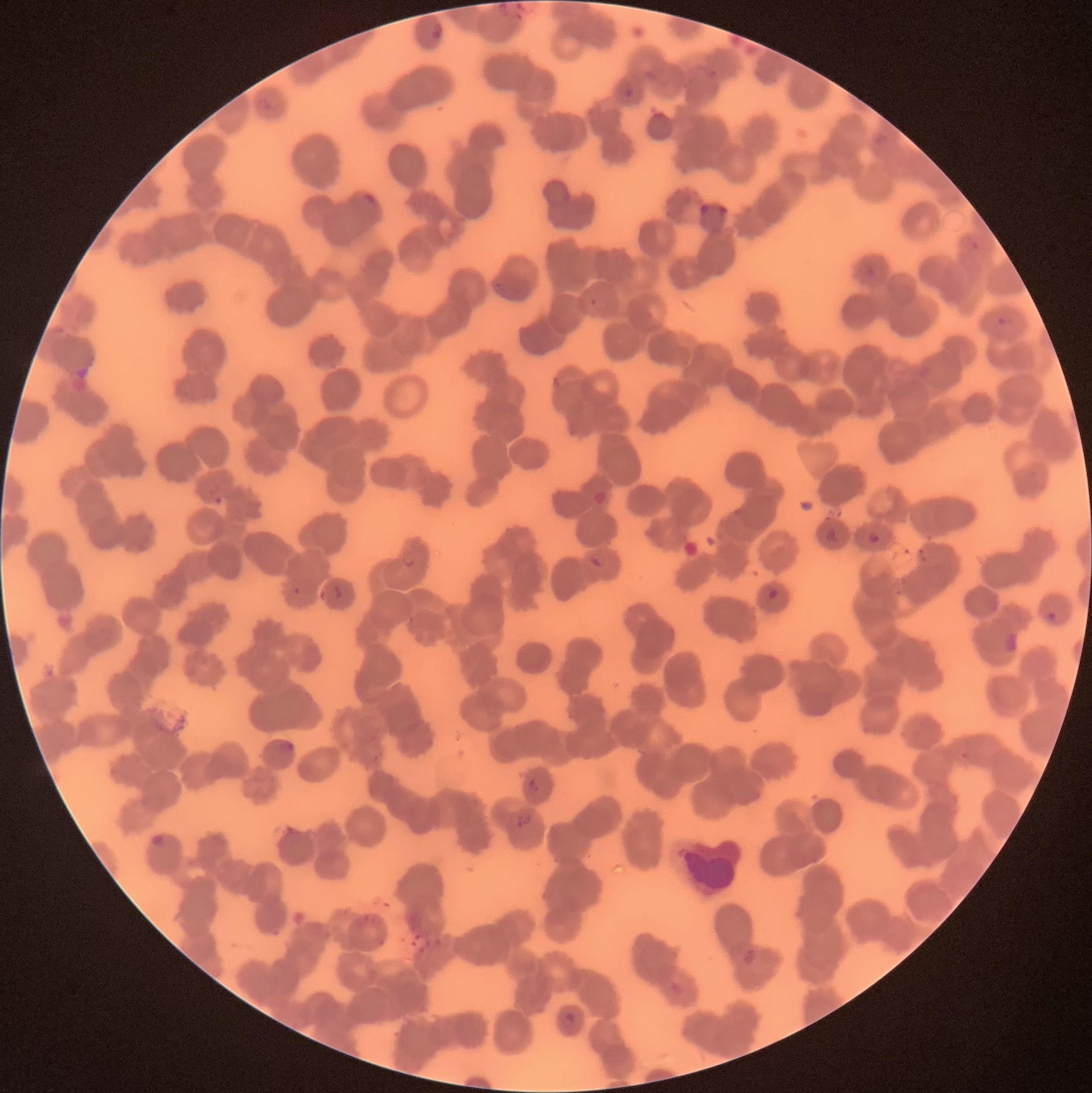

coordinate format = approximate bounding boxes as named x1/y1/x2/y2 corners in pixels
Plasmodium parasite locations = (x1=496, y1=2, x2=513, y2=18), (x1=430, y1=23, x2=444, y2=41), (x1=702, y1=64, x2=719, y2=79), (x1=615, y1=81, x2=635, y2=99), (x1=363, y1=191, x2=380, y2=207), (x1=994, y1=315, x2=1016, y2=328), (x1=550, y1=375, x2=563, y2=389), (x1=208, y1=487, x2=224, y2=505), (x1=823, y1=528, x2=839, y2=544), (x1=866, y1=530, x2=883, y2=546), (x1=401, y1=552, x2=417, y2=567), (x1=585, y1=553, x2=607, y2=570), (x1=332, y1=583, x2=344, y2=600), (x1=292, y1=586, x2=303, y2=596), (x1=765, y1=587, x2=780, y2=601), (x1=1045, y1=611, x2=1058, y2=622), (x1=1001, y1=630, x2=1020, y2=655), (x1=278, y1=740, x2=294, y2=751), (x1=528, y1=778, x2=539, y2=793), (x1=515, y1=813, x2=533, y2=828), (x1=152, y1=833, x2=165, y2=846), (x1=743, y1=948, x2=757, y2=964), (x1=561, y1=1012, x2=578, y2=1033)
image size = 1092×1093 pixels
red blood cell morphology = rouleaux formation
modality = optical microscopy
preparation = thin blood film